Assess this cell for malaria.
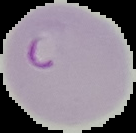
It is parasitized.

image size = 136×133 pixels
image type = cell region segmented out of the field of view; surrounding area masked to black
preparation = thin blood film